Locate every blood parasite and identify its species.
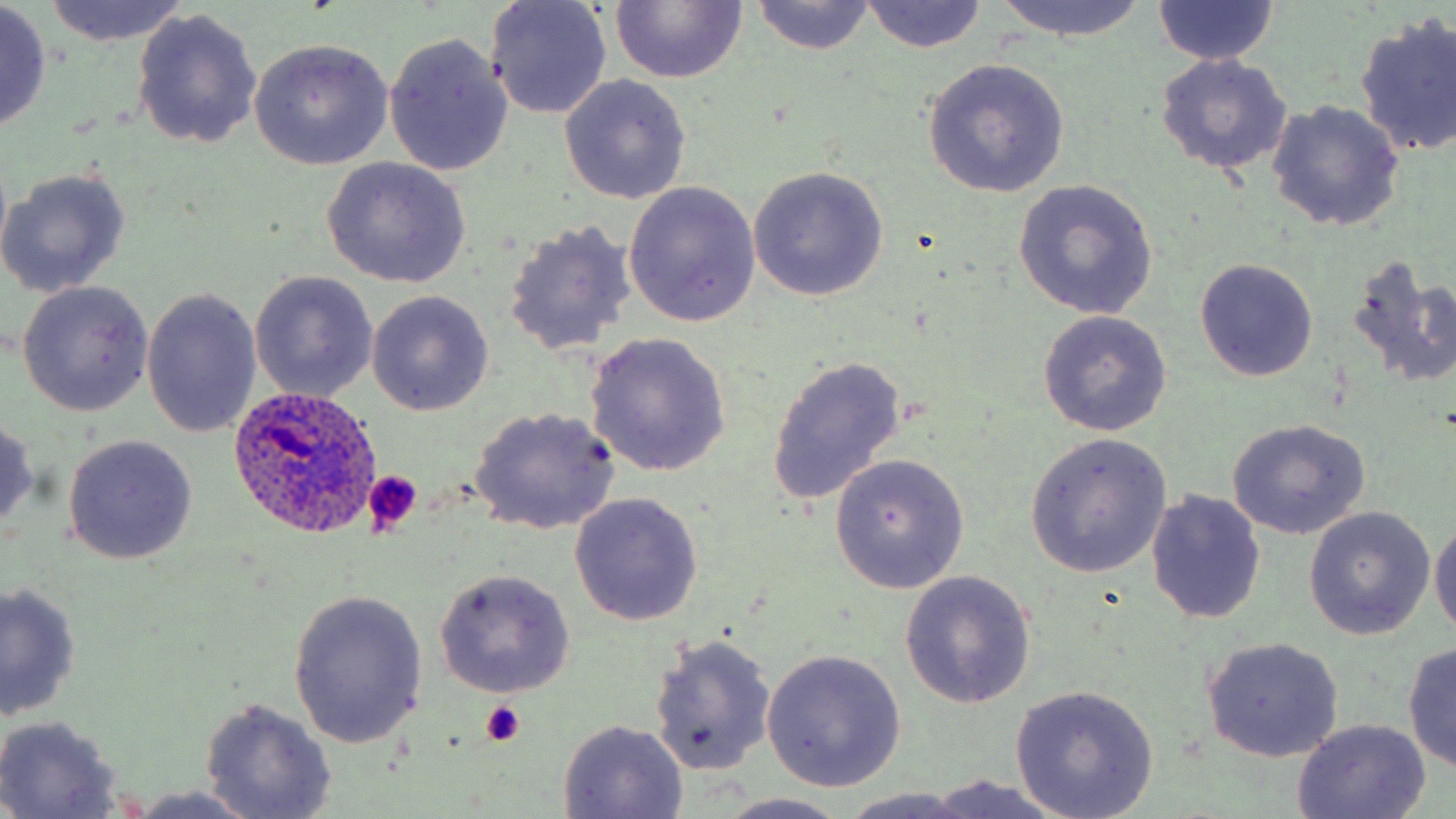

Approximate bounding boxes as (x1, y1, x2, y2) in pixels.
Plasmodium ovale-infected red blood cells: (228, 383, 382, 537).
No Plasmodium falciparum, Plasmodium malariae, Plasmodium vivax, Babesia divergens, or Trypanosoma brucei observed.

{
  "slide_level_diagnosis": "Plasmodium ovale",
  "uninfected_red_blood_cell_locations": "approximate bounding boxes as (x1, y1, x2, y2) in pixels: (39, 0, 188, 46), (609, 0, 747, 84), (991, 0, 1148, 42), (1150, 0, 1280, 68), (483, 1, 613, 120), (748, 1, 878, 55), (858, 2, 989, 53), (0, 3, 52, 132), (132, 8, 264, 150), (1354, 13, 1456, 158), (383, 33, 514, 177), (247, 39, 394, 172), (1154, 53, 1294, 175), (922, 56, 1071, 198), (558, 76, 691, 206), (1266, 100, 1406, 232), (319, 156, 472, 288), (747, 165, 887, 303), (1, 169, 132, 298), (1013, 180, 1159, 320), (624, 182, 763, 326), (501, 222, 635, 357), (1345, 254, 1453, 387), (1195, 259, 1319, 381), (250, 271, 378, 403), (16, 281, 154, 416), (143, 289, 263, 438), (367, 290, 494, 415), (1036, 310, 1172, 435), (584, 332, 732, 477), (766, 353, 909, 510), (469, 407, 620, 535), (0, 415, 41, 538), (1226, 418, 1371, 539), (1024, 433, 1172, 579), (63, 435, 198, 565), (829, 454, 970, 593), (1146, 490, 1267, 624), (569, 492, 704, 627), (1304, 507, 1434, 639), (1430, 518, 1456, 640), (433, 569, 575, 698), (900, 571, 1037, 709), (1, 581, 80, 723), (286, 590, 426, 748), (648, 634, 777, 778), (1202, 636, 1345, 761), (1403, 641, 1456, 770), (762, 649, 908, 792), (1010, 684, 1159, 818), (200, 698, 337, 818), (0, 715, 125, 817), (1292, 718, 1432, 818), (556, 720, 690, 818), (924, 775, 1065, 819), (117, 786, 268, 819), (838, 789, 989, 818), (710, 792, 858, 819)",
  "modality": "light microscopy",
  "magnification": "1000x",
  "image_size": "1456×819 pixels",
  "field_of_view": "one of a larger specimen",
  "stain": "May-Grünwald-Giemsa",
  "preparation": "thin blood film",
  "platelet_locations": "approximate bounding boxes as (x1, y1, x2, y2) in pixels: (363, 471, 422, 535), (479, 699, 527, 746)"
}